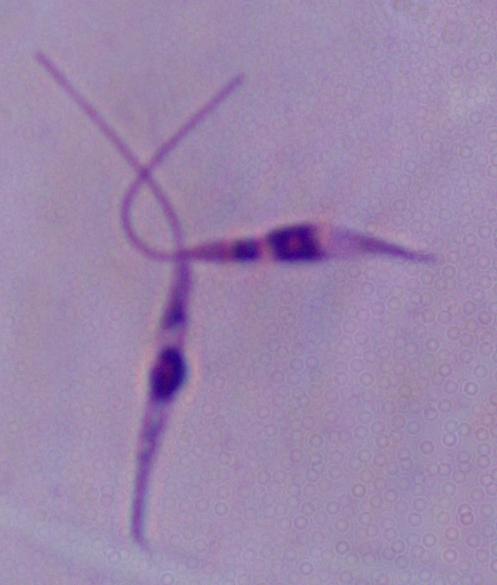 A Leishmania parasite is seen. Micrograph. 1000x magnification.